Assess this cell for malaria.
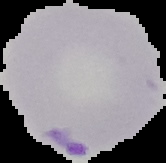
Parasitized.

Summary:
  - Preparation: thin blood film
  - Image size: 166×163 pixels
  - Image type: segmented cell region with the area outside set to black